Describe the morphology of the red blood cells.
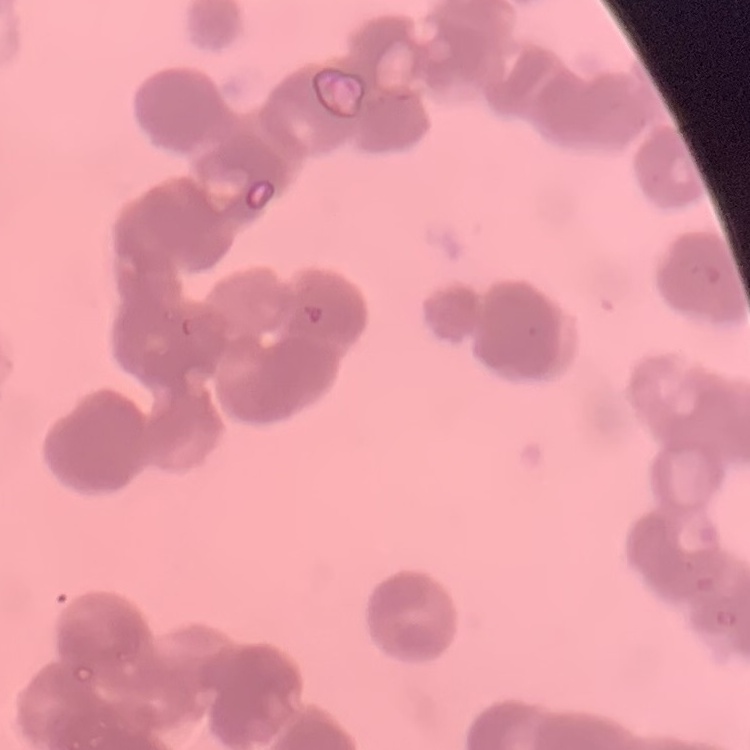

Rouleaux formation.

Summary:
  - Image type: square crop of a larger photomicrograph
  - Preparation: thin blood film
  - Stain: Field's or Giemsa